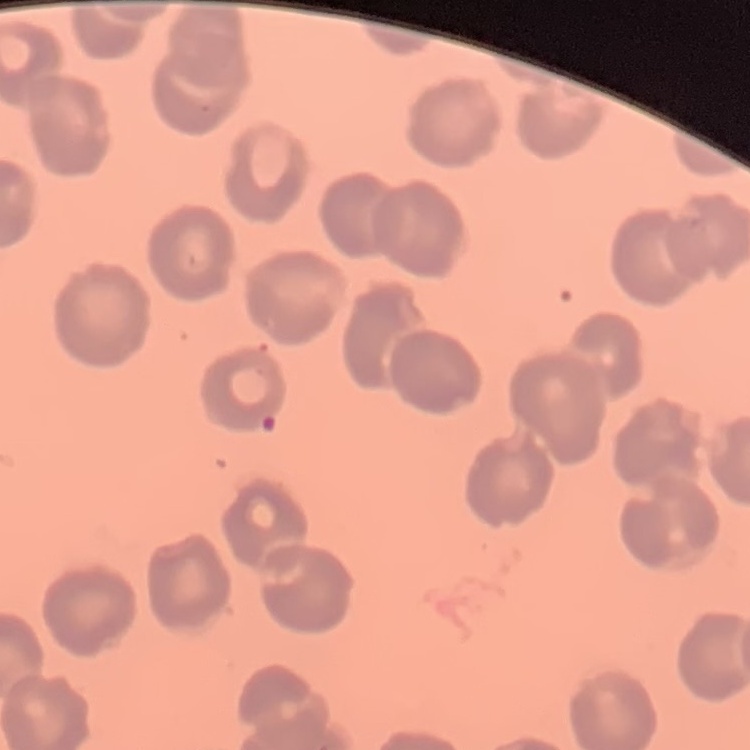
The red blood cells show no rouleaux formation. Thin blood smear. Field's or Giemsa stain. Square crop of a larger photomicrograph.